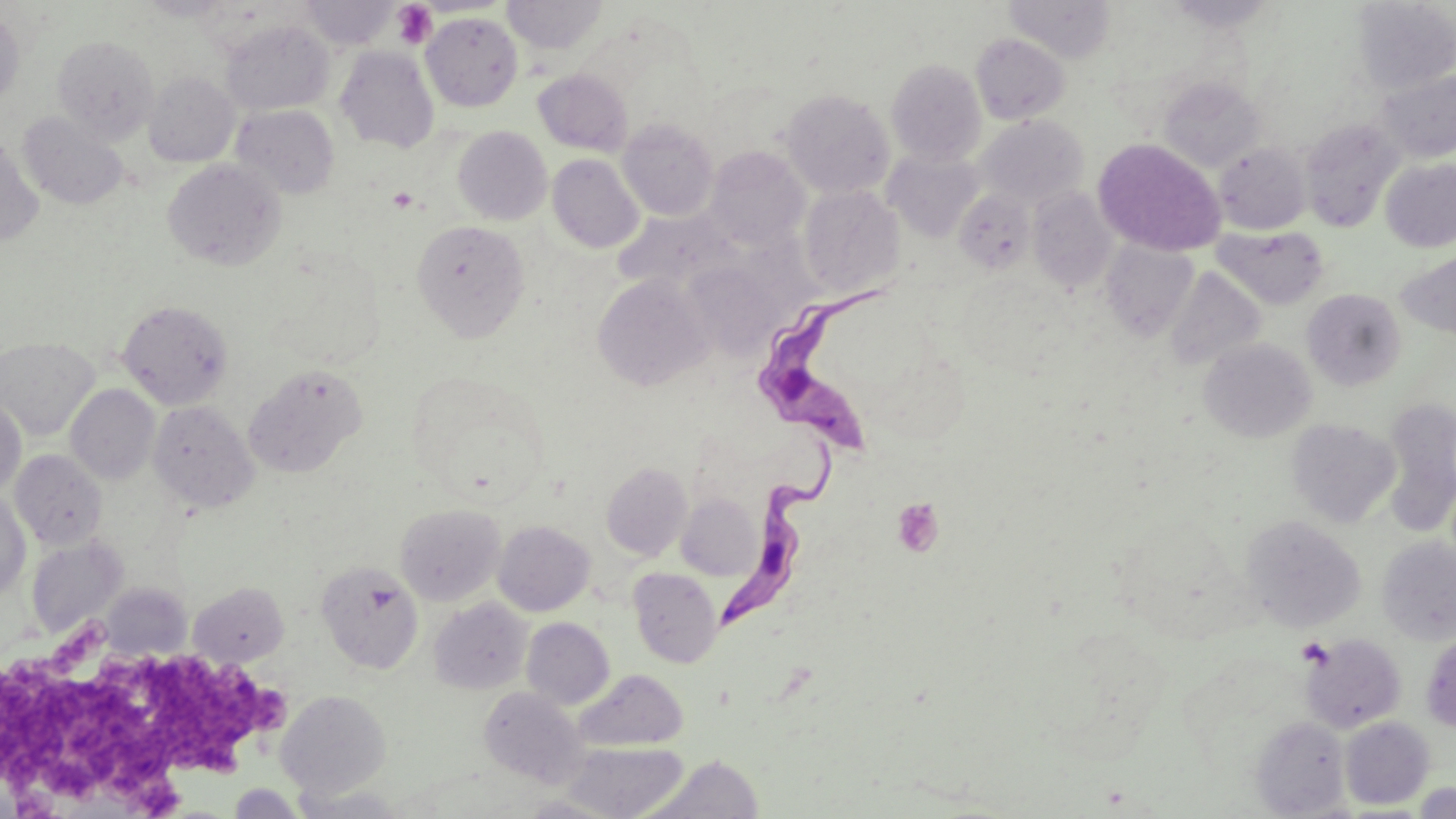
slide-level diagnosis = Trypanosoma brucei
field of view = single
stain = May-Grünwald-Giemsa
magnification = 1000x
platelet locations = approximate bounding boxes as (x1, y1, x2, y2) in pixels: (392, 2, 437, 50), (387, 186, 421, 213), (891, 496, 945, 557), (0, 653, 180, 816), (146, 655, 269, 773), (247, 682, 287, 735)
uninfected red blood cell locations = approximate bounding boxes as (x1, y1, x2, y2) in pixels: (140, 0, 234, 21), (301, 0, 399, 50), (503, 0, 607, 55), (1005, 0, 1115, 62), (1162, 0, 1279, 32), (1351, 1, 1455, 94), (0, 9, 25, 109), (421, 13, 522, 110), (221, 20, 335, 115), (970, 33, 1069, 123), (52, 35, 159, 143), (335, 46, 439, 153), (886, 59, 986, 166), (533, 69, 633, 155), (1375, 70, 1456, 163), (143, 71, 240, 168), (1158, 76, 1264, 171), (780, 89, 895, 198), (231, 104, 340, 199), (18, 111, 128, 210), (977, 114, 1088, 206), (618, 118, 719, 220), (1300, 119, 1403, 232), (452, 126, 552, 225), (0, 135, 42, 247), (1093, 138, 1225, 256), (1214, 142, 1311, 234), (705, 146, 810, 250), (882, 149, 985, 242), (547, 154, 644, 253), (162, 159, 287, 271), (1380, 159, 1456, 252), (799, 185, 904, 299), (1027, 186, 1118, 291), (953, 187, 1035, 274), (615, 208, 738, 296), (411, 220, 530, 341), (1213, 225, 1329, 309), (1101, 241, 1198, 340), (1397, 250, 1456, 340), (681, 261, 779, 359), (1164, 267, 1266, 372), (592, 274, 712, 391), (1302, 288, 1406, 390), (117, 299, 234, 410), (0, 337, 99, 441), (1198, 338, 1317, 442), (244, 364, 366, 477), (66, 384, 160, 485), (0, 397, 27, 498), (1382, 397, 1456, 532), (148, 400, 258, 512), (1286, 418, 1401, 528), (10, 449, 107, 550), (601, 462, 692, 561), (0, 491, 31, 602), (676, 493, 760, 580), (395, 503, 505, 605), (1241, 515, 1366, 632), (493, 520, 595, 616), (26, 536, 127, 637), (1376, 537, 1456, 645), (317, 561, 424, 674), (628, 568, 723, 668), (189, 582, 289, 666), (101, 583, 190, 659), (429, 598, 533, 695), (521, 618, 614, 709), (1420, 630, 1456, 734), (1299, 633, 1407, 733), (577, 669, 687, 751), (479, 686, 587, 787), (275, 690, 391, 799), (1250, 716, 1351, 817), (1340, 716, 1434, 809), (560, 741, 689, 819), (640, 754, 765, 819), (1412, 782, 1456, 818), (227, 784, 307, 818), (293, 785, 412, 818), (519, 794, 624, 818)
preparation = thin blood film
modality = light microscopy
image size = 1456×819 pixels
Trypanosoma brucei locations = approximate bounding boxes as (x1, y1, x2, y2) in pixels: (759, 277, 897, 463), (717, 436, 845, 636)